Assess the morphology of the erythrocytes.
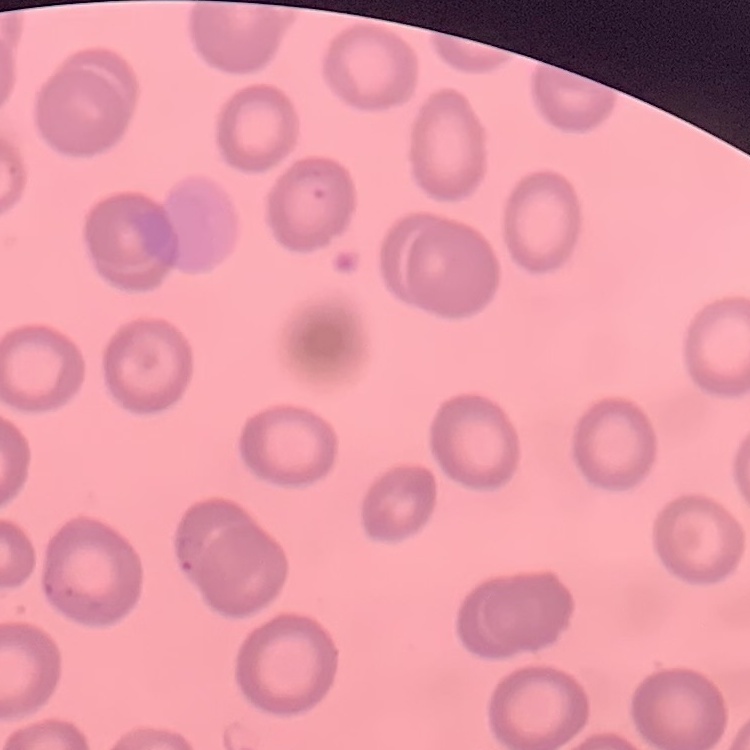
They show no rouleaux formation.

Summary:
  - Preparation: thin blood smear
  - Stain: Field's or Giemsa
  - Image type: square crop of a larger photomicrograph